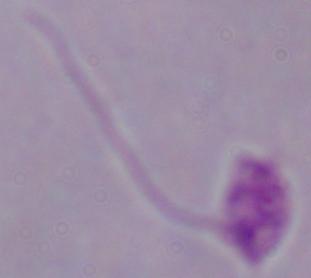
Summary:
  - Magnification: 1000x
  - Identification: Leishmania
  - Modality: micrograph